Locate every Plasmodium parasite.
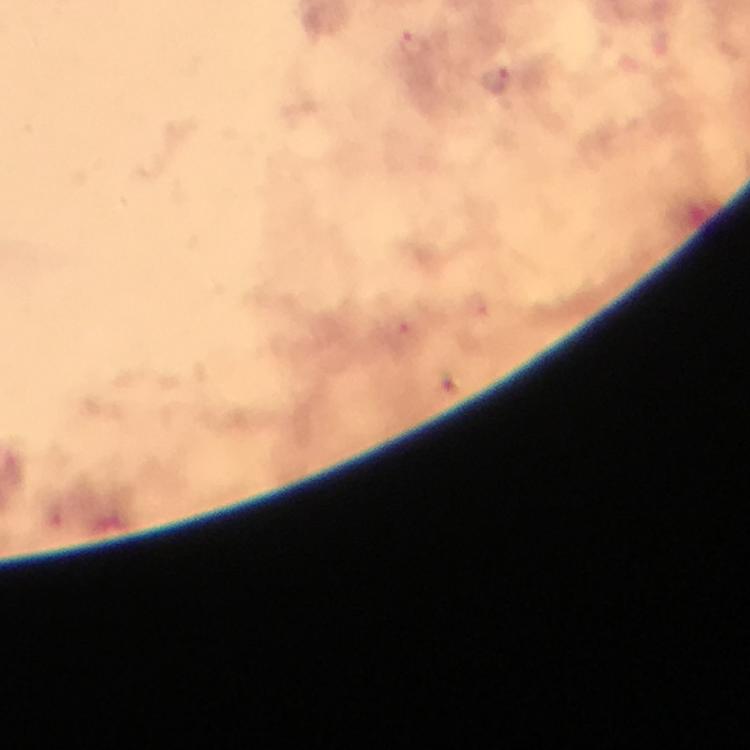

Approximate centers as [x, y] in pixels.
Plasmodium parasites: [417, 45], [495, 84], [401, 332].

preparation = thick blood smear
stain = Giemsa
immersion oil = applied
magnification = 100x
cropped from = one field of view
context = from a malaria diagnostic workup
capture = smartphone photograph through a microscope
image size = 750×750 pixels